Classify this cell by malaria status.
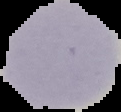

It is uninfected.

image size = 121×112 pixels
preparation = thin blood smear
image type = segmented cell region on a black background